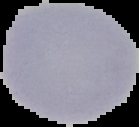

{
  "result": "no Plasmodium parasites seen",
  "preparation": "thin blood smear",
  "image_type": "segmented cell region on a black background",
  "image_size": "139×127 pixels"
}